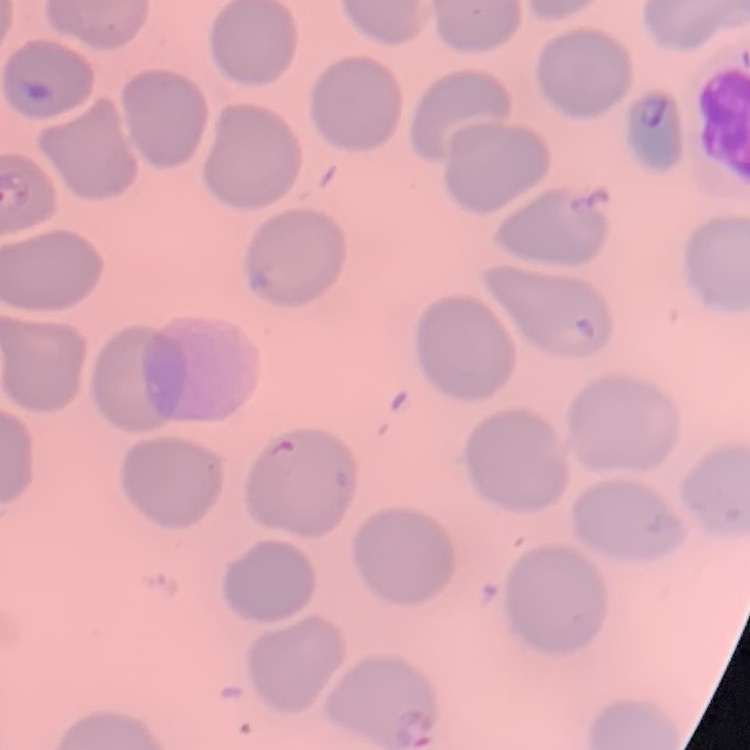 The red blood cells exhibit no rouleaux formation. Square crop of a larger photomicrograph. Thin blood film. Stained with either Field's or Giemsa.